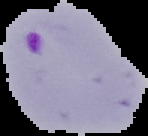

Summary:
  - Preparation: thin blood smear
  - Result: malaria parasites identified
  - Image size: 148×136 pixels
  - Image type: segmented cell region on a black background